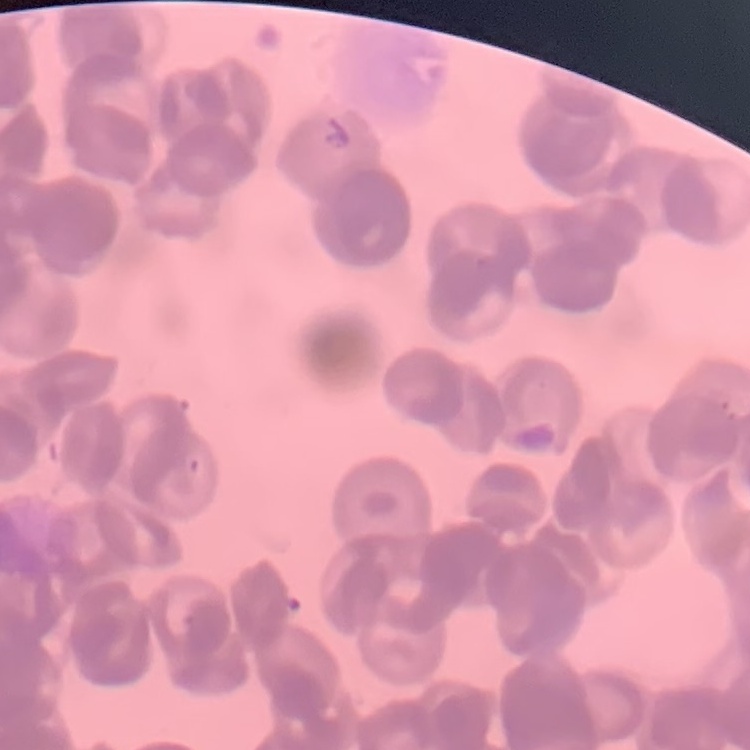

red blood cell morphology = rouleaux formation
image type = square crop of a larger photomicrograph
preparation = thin blood film
stain = Field's or Giemsa